State which parasite is depicted.
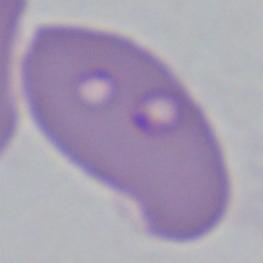

Babesia.

{
  "modality": "micrograph",
  "magnification": "1000x"
}